Give the preparation type.
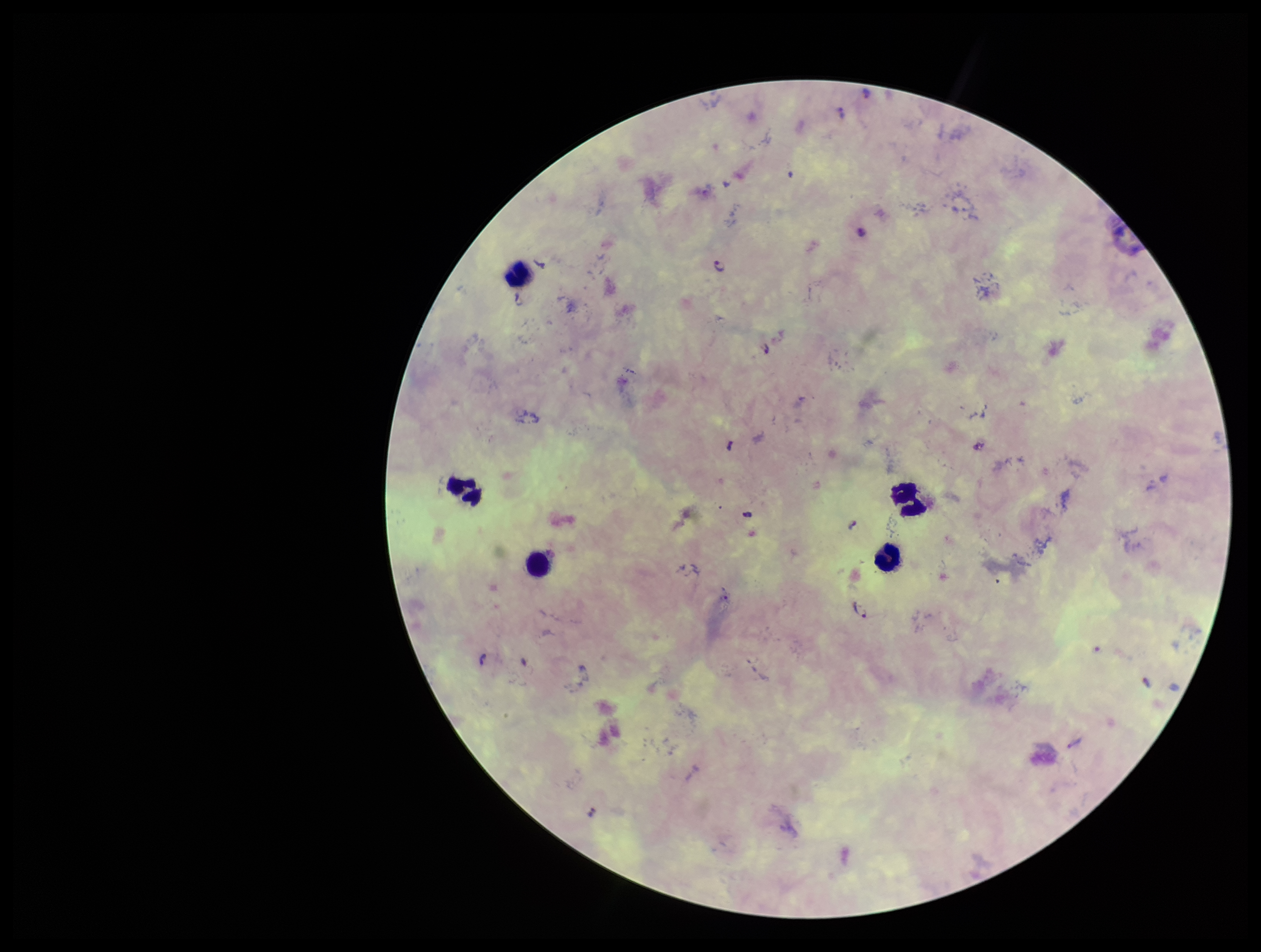

It is a thick blood smear.

parasite count = 11
species reported for this patient = Plasmodium falciparum
leukocyte count = 5
Plasmodium parasites = seen
stain = Giemsa
patient malaria status = infected
field of view = single
image size = 1261×952 pixels
capture = smartphone photograph through the microscope eyepiece